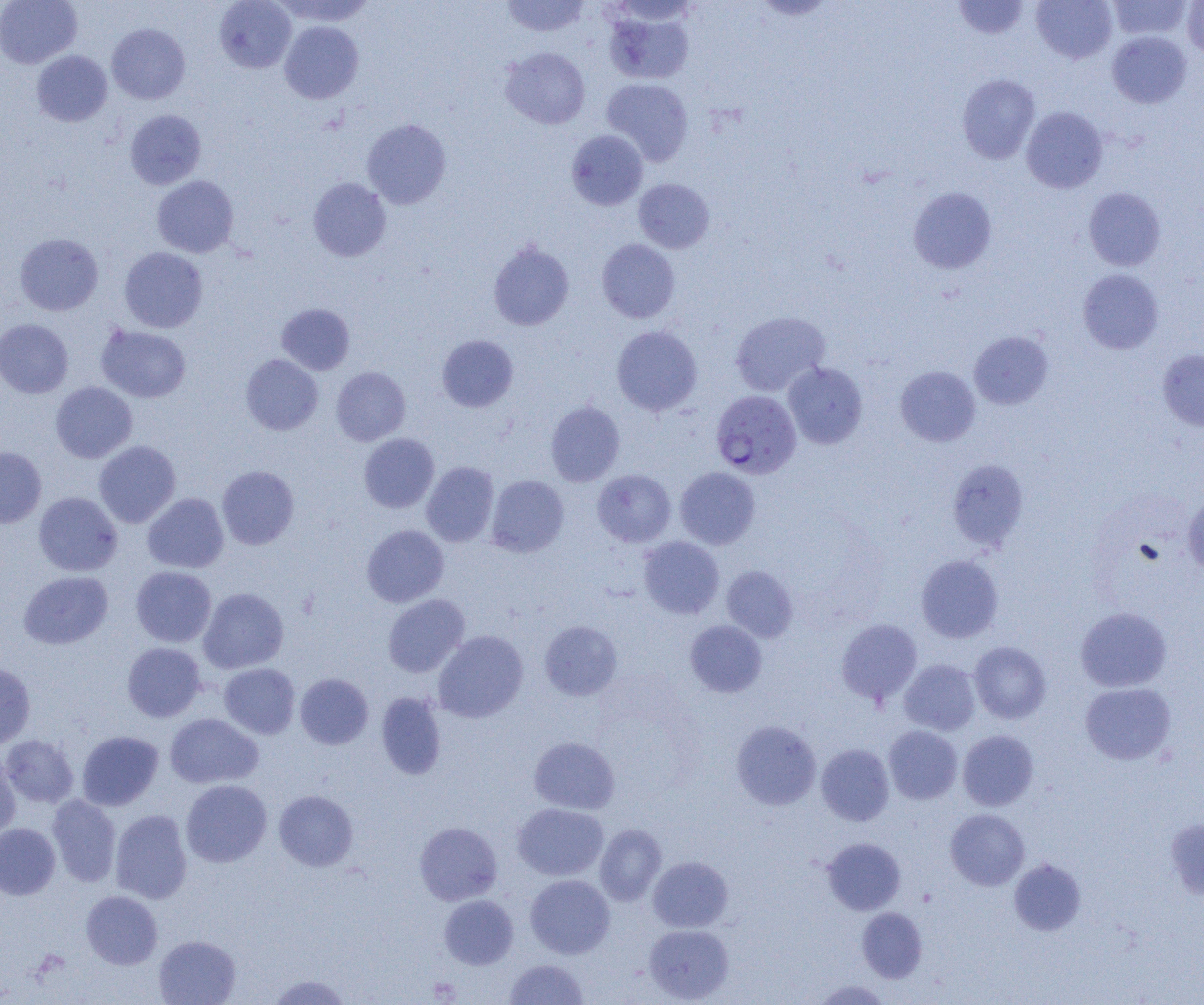
Summary:
  - Coordinate format: approximate bounding boxes as named x1/y1/x2/y2 corners in pixels
  - Plasmodium falciparum-infected red blood cell locations: (x1=710, y1=389, x2=802, y2=479)
  - Uninfected red blood cell locations: (x1=0, y1=0, x2=82, y2=68), (x1=214, y1=0, x2=296, y2=73), (x1=274, y1=0, x2=375, y2=25), (x1=501, y1=0, x2=590, y2=37), (x1=954, y1=0, x2=1030, y2=39), (x1=1031, y1=0, x2=1117, y2=64), (x1=1108, y1=0, x2=1192, y2=41), (x1=1182, y1=1, x2=1204, y2=57), (x1=602, y1=5, x2=696, y2=85), (x1=279, y1=21, x2=363, y2=104), (x1=107, y1=23, x2=190, y2=104), (x1=1107, y1=31, x2=1192, y2=108), (x1=500, y1=47, x2=590, y2=130), (x1=31, y1=50, x2=112, y2=127), (x1=957, y1=73, x2=1041, y2=163), (x1=601, y1=78, x2=693, y2=166), (x1=1021, y1=107, x2=1108, y2=193), (x1=125, y1=109, x2=206, y2=189), (x1=362, y1=118, x2=451, y2=209), (x1=566, y1=130, x2=647, y2=210), (x1=152, y1=175, x2=238, y2=257), (x1=308, y1=177, x2=391, y2=262), (x1=634, y1=179, x2=714, y2=253), (x1=908, y1=186, x2=997, y2=275), (x1=1083, y1=187, x2=1165, y2=271), (x1=14, y1=233, x2=104, y2=316), (x1=597, y1=239, x2=680, y2=323), (x1=488, y1=240, x2=575, y2=330), (x1=119, y1=247, x2=208, y2=332), (x1=1078, y1=269, x2=1163, y2=354), (x1=276, y1=303, x2=355, y2=375), (x1=730, y1=311, x2=831, y2=397), (x1=0, y1=318, x2=73, y2=398), (x1=96, y1=325, x2=191, y2=403), (x1=612, y1=326, x2=702, y2=416), (x1=969, y1=331, x2=1053, y2=410), (x1=436, y1=334, x2=518, y2=412), (x1=1158, y1=349, x2=1204, y2=432), (x1=240, y1=354, x2=323, y2=435), (x1=783, y1=362, x2=868, y2=449), (x1=331, y1=366, x2=411, y2=446), (x1=895, y1=366, x2=980, y2=446), (x1=50, y1=381, x2=137, y2=463), (x1=545, y1=401, x2=625, y2=486), (x1=358, y1=433, x2=439, y2=513), (x1=94, y1=440, x2=181, y2=528), (x1=0, y1=447, x2=46, y2=527), (x1=947, y1=459, x2=1029, y2=551), (x1=421, y1=462, x2=499, y2=547), (x1=217, y1=465, x2=299, y2=549), (x1=675, y1=466, x2=760, y2=549), (x1=592, y1=469, x2=675, y2=547), (x1=486, y1=475, x2=569, y2=557), (x1=33, y1=492, x2=122, y2=576), (x1=142, y1=493, x2=229, y2=573), (x1=1182, y1=494, x2=1204, y2=576), (x1=362, y1=525, x2=449, y2=607), (x1=638, y1=536, x2=724, y2=619), (x1=916, y1=554, x2=1003, y2=643), (x1=131, y1=566, x2=216, y2=647), (x1=722, y1=566, x2=798, y2=642), (x1=19, y1=571, x2=113, y2=649), (x1=199, y1=587, x2=289, y2=673), (x1=383, y1=594, x2=469, y2=677), (x1=1075, y1=606, x2=1172, y2=692), (x1=836, y1=618, x2=923, y2=705), (x1=539, y1=620, x2=622, y2=700), (x1=685, y1=620, x2=767, y2=697), (x1=433, y1=630, x2=528, y2=722), (x1=969, y1=641, x2=1051, y2=724), (x1=122, y1=642, x2=206, y2=722), (x1=899, y1=659, x2=981, y2=735), (x1=219, y1=663, x2=300, y2=739), (x1=0, y1=664, x2=35, y2=750), (x1=295, y1=673, x2=374, y2=749), (x1=1080, y1=682, x2=1177, y2=765), (x1=376, y1=692, x2=446, y2=779), (x1=165, y1=713, x2=263, y2=788), (x1=731, y1=720, x2=821, y2=810), (x1=883, y1=725, x2=963, y2=804), (x1=958, y1=729, x2=1038, y2=810), (x1=77, y1=730, x2=164, y2=810), (x1=1, y1=735, x2=79, y2=808), (x1=529, y1=736, x2=620, y2=814), (x1=816, y1=743, x2=894, y2=825), (x1=0, y1=753, x2=20, y2=841), (x1=181, y1=780, x2=272, y2=867), (x1=274, y1=790, x2=358, y2=871), (x1=47, y1=795, x2=121, y2=887), (x1=513, y1=803, x2=609, y2=880), (x1=110, y1=809, x2=192, y2=904), (x1=945, y1=809, x2=1029, y2=890), (x1=1164, y1=818, x2=1204, y2=900), (x1=414, y1=821, x2=502, y2=905), (x1=0, y1=823, x2=60, y2=899), (x1=595, y1=824, x2=666, y2=906), (x1=822, y1=837, x2=906, y2=914), (x1=648, y1=856, x2=733, y2=932), (x1=1009, y1=859, x2=1086, y2=935), (x1=525, y1=874, x2=614, y2=958), (x1=81, y1=890, x2=162, y2=969), (x1=439, y1=895, x2=518, y2=969), (x1=857, y1=907, x2=927, y2=982), (x1=644, y1=924, x2=734, y2=1003), (x1=154, y1=935, x2=240, y2=1005), (x1=504, y1=958, x2=589, y2=1004), (x1=265, y1=973, x2=354, y2=1004), (x1=811, y1=979, x2=891, y2=1004)
  - Slide-level diagnosis: Plasmodium falciparum
  - Magnification: 1000x
  - Field of view: one of a larger specimen
  - Image size: 1204×1005 pixels
  - Preparation: thin blood smear
  - Modality: optical microscopy